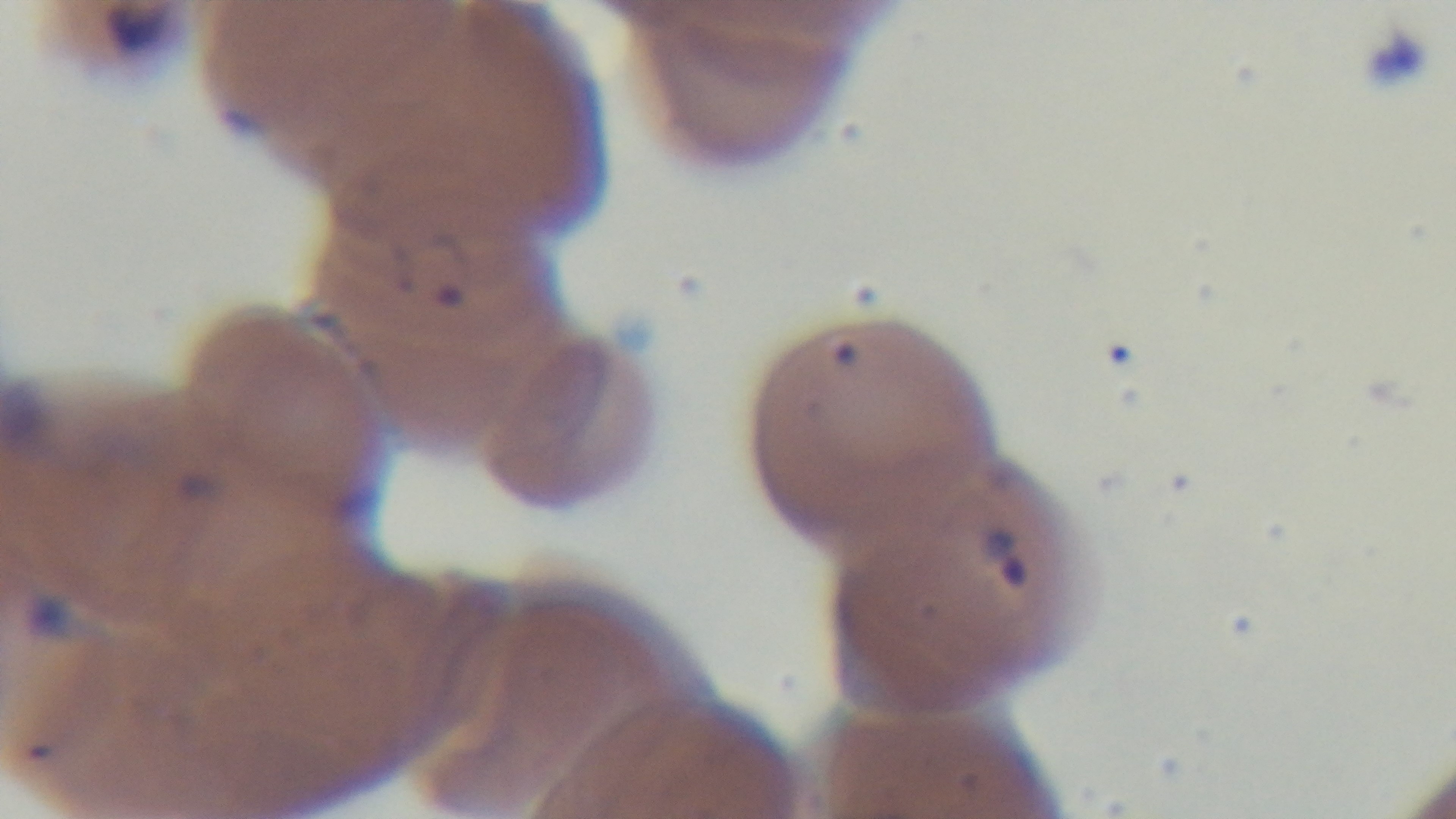
Summary:
  - Modality: light microscopy
  - Malaria status: positive
  - Capture: mounted 4K digital camera
  - Objective: 100x oil immersion
  - Stain: Giemsa
  - Field of view: one from the slide
  - Preparation: thin smear